Outline each uninfected red blood cell.
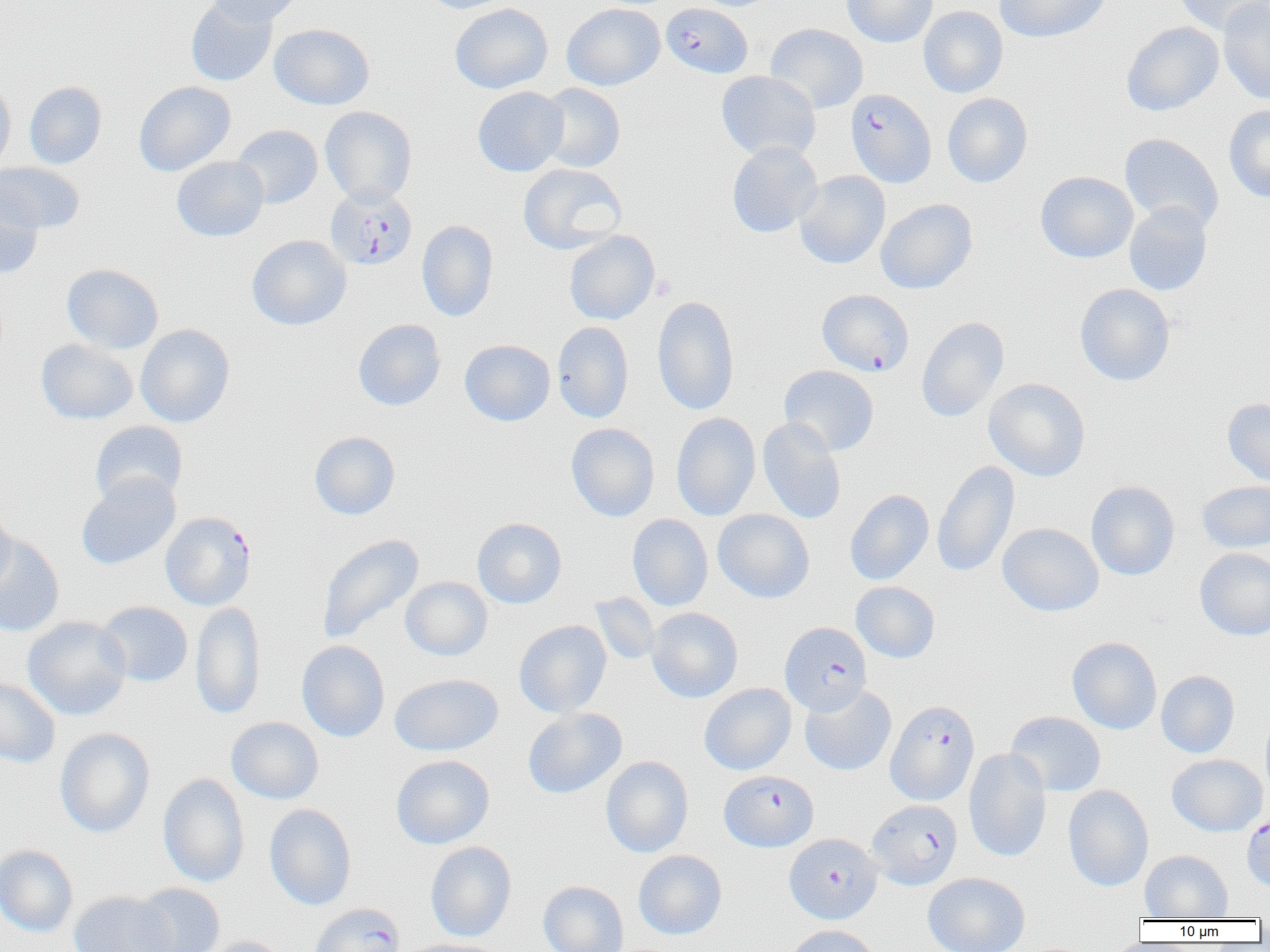
Approximate bounding boxes as (x1,y1)-(x2,y2) corner pairs in pixels.
Uninfected red blood cells: (186,0)-(277,86), (207,0)-(302,26), (420,0)-(514,13), (842,0)-(937,48), (994,0)-(1111,44), (1172,0)-(1270,36), (1218,0)-(1270,105), (450,3)-(552,93), (561,3)-(665,90), (918,6)-(1008,98), (1121,21)-(1224,116), (269,23)-(375,110), (765,23)-(868,113), (716,70)-(820,161), (0,77)-(16,176), (134,81)-(235,176), (24,82)-(106,169), (536,83)-(625,172), (472,86)-(568,177), (942,93)-(1033,187), (1224,105)-(1270,203), (320,106)-(417,206), (231,124)-(323,209), (1120,133)-(1224,232), (727,142)-(822,237), (172,156)-(269,241), (0,161)-(86,233), (517,163)-(627,255), (794,171)-(890,269), (1035,171)-(1138,263), (0,190)-(43,278), (876,198)-(977,294), (1124,202)-(1213,295), (417,220)-(498,321), (564,230)-(660,325), (247,235)-(351,330), (62,264)-(164,354), (1075,283)-(1175,386), (652,295)-(740,415), (916,316)-(1009,423), (353,319)-(445,410), (553,321)-(634,423), (135,324)-(235,427), (36,339)-(138,424), (459,339)-(555,426), (779,365)-(879,456), (983,378)-(1091,481), (1222,398)-(1270,487), (671,412)-(761,521), (757,417)-(847,524), (89,421)-(188,506), (566,423)-(659,522), (309,431)-(400,520), (932,460)-(1019,577), (76,472)-(180,570), (1197,480)-(1270,553), (1086,481)-(1180,581), (845,489)-(934,585), (0,505)-(16,595), (713,509)-(815,603), (627,514)-(713,611), (472,517)-(567,608), (997,523)-(1103,616), (316,534)-(424,645), (0,535)-(65,636), (1194,547)-(1270,640), (400,576)-(493,661), (851,581)-(939,663), (590,595)-(660,665), (96,601)-(193,687), (190,602)-(265,720), (646,607)-(743,702), (22,616)-(132,720), (514,620)-(612,718), (1066,636)-(1162,734), (296,640)-(390,742), (1156,670)-(1240,758), (389,673)-(503,756), (0,676)-(60,768), (699,683)-(796,775), (799,684)-(897,776), (1260,705)-(1270,803), (522,707)-(627,799), (1005,711)-(1106,797), (226,717)-(324,804), (54,728)-(155,838), (964,748)-(1051,862), (1167,754)-(1268,836), (391,755)-(494,849), (601,756)-(693,858), (158,773)-(249,888), (1063,785)-(1153,891), (264,804)-(357,910), (425,841)-(516,941), (0,844)-(78,937), (633,850)-(727,940), (1140,850)-(1233,920), (923,872)-(1030,952), (538,881)-(629,952), (131,882)-(225,952), (69,891)-(176,952), (784,925)-(881,952), (200,936)-(292,952), (395,938)-(505,952).

plasmodium_falciparum_infected_red_blood_cell_locations: 'approximate bounding boxes as (x1,y1)-(x2,y2) corner pairs in pixels: (661,2)-(753,78), (845,88)-(936,188), (325,187)-(417,271), (817,289)-(913,376), (160,511)-(256,610), (779,622)-(872,714), (886,699)-(979,806), (719,770)-(818,852), (867,799)-(963,890), (1241,810)-(1270,892), (784,833)-(882,924), (310,902)-(405,952)'
slide_level_diagnosis: Plasmodium falciparum
image_size: 1270×952 pixels
preparation: thin blood film
field_of_view: single
modality: optical microscopy
magnification: 1000x